Describe the morphology of the erythrocytes.
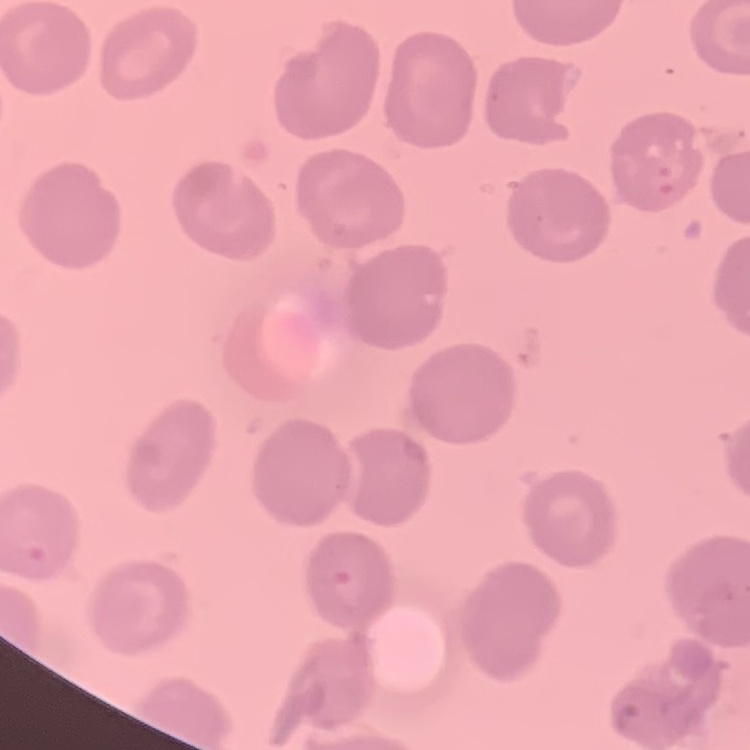

They show no rouleaux formation.

Summary:
  - Preparation: thin peripheral smear
  - Image type: one tile cut from a larger photomicrograph
  - Stain: Field's or Giemsa